Comment on the morphology of the erythrocytes.
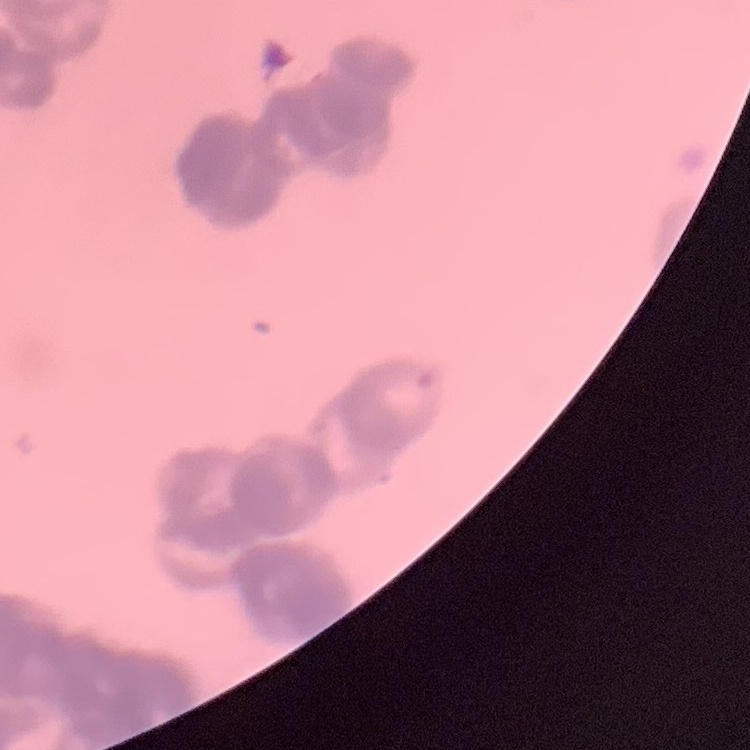

They show rouleaux formation.

Summary:
  - Stain: Field's or Giemsa
  - Preparation: thin peripheral smear
  - Image type: square crop of a larger photomicrograph